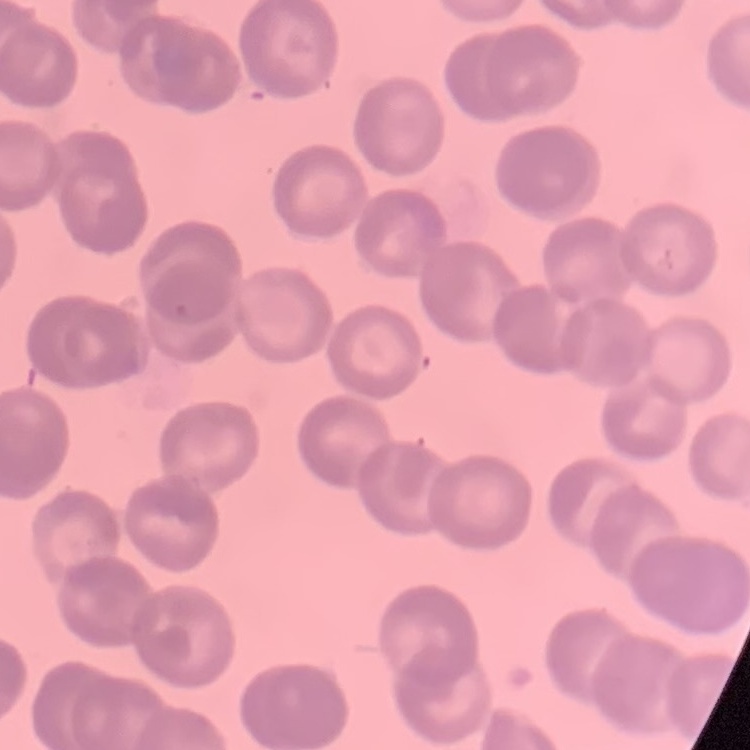

erythrocyte morphology = rouleaux formation
preparation = thin blood smear
image type = square crop of a larger photomicrograph
stain = Field's or Giemsa